Classify this cell by malaria status.
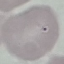

It is uninfected.

Giemsa stain. Thin blood film. Cell patch, automatically extracted from a larger field of view and resized to 64 × 64 pixels. Acquired by smartphone through the microscope eyepiece.